State which parasite is depicted.
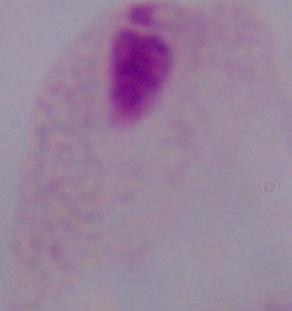

A trichomonad.

Micrograph. Captured at 1000x magnification.